Point out each malaria parasite and classify it by life-cycle stage.
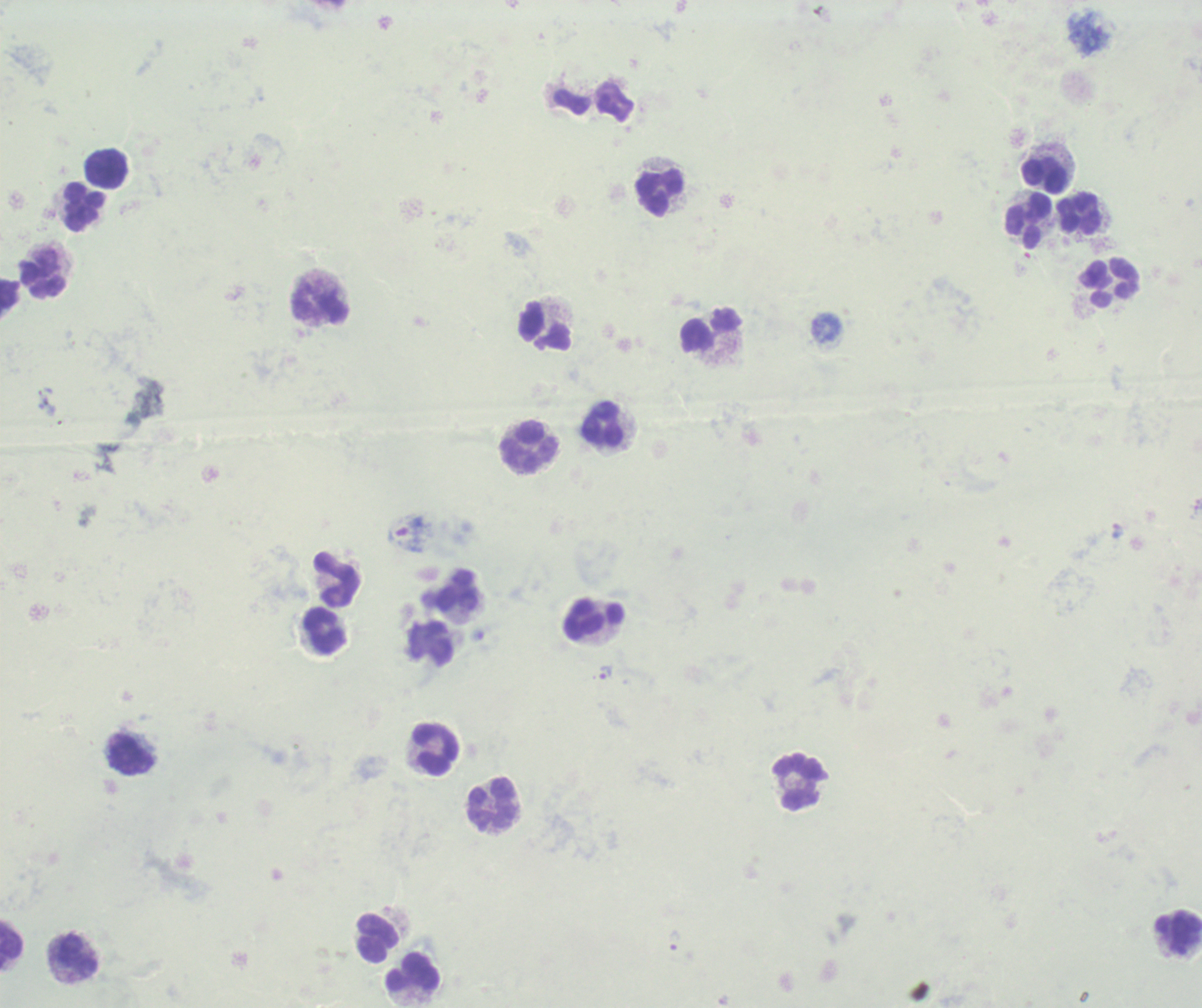
Approximate centers as [x, y] in pixels.
Trophozoites: [605, 672], [674, 940], [77, 957].
No schizont or gametocyte forms observed.

Approximate centers as [x, y] in pixels. Leukocyte locations: [105, 169], [1042, 174], [660, 192], [84, 205], [1079, 214], [1028, 222], [40, 274], [1109, 283], [319, 305], [545, 326], [711, 331], [602, 424], [529, 447], [335, 578], [458, 592], [594, 616], [325, 631], [435, 749], [130, 753], [801, 781], [493, 805], [376, 939], [11, 945], [414, 972]. Previously used in a real diagnosis. Image is 1202×1008 pixels. Background quality: poor. Single field of view. 100x magnification. Thick smear of blood. Romanowsky-stained preparation.